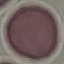
Summary:
  - Result: no malaria parasites seen
  - Capture: smartphone camera at the microscope eyepiece
  - Stain: Giemsa
  - Preparation: thin blood smear
  - Image type: automatically extracted cell patch, resized to 64 × 64 pixels